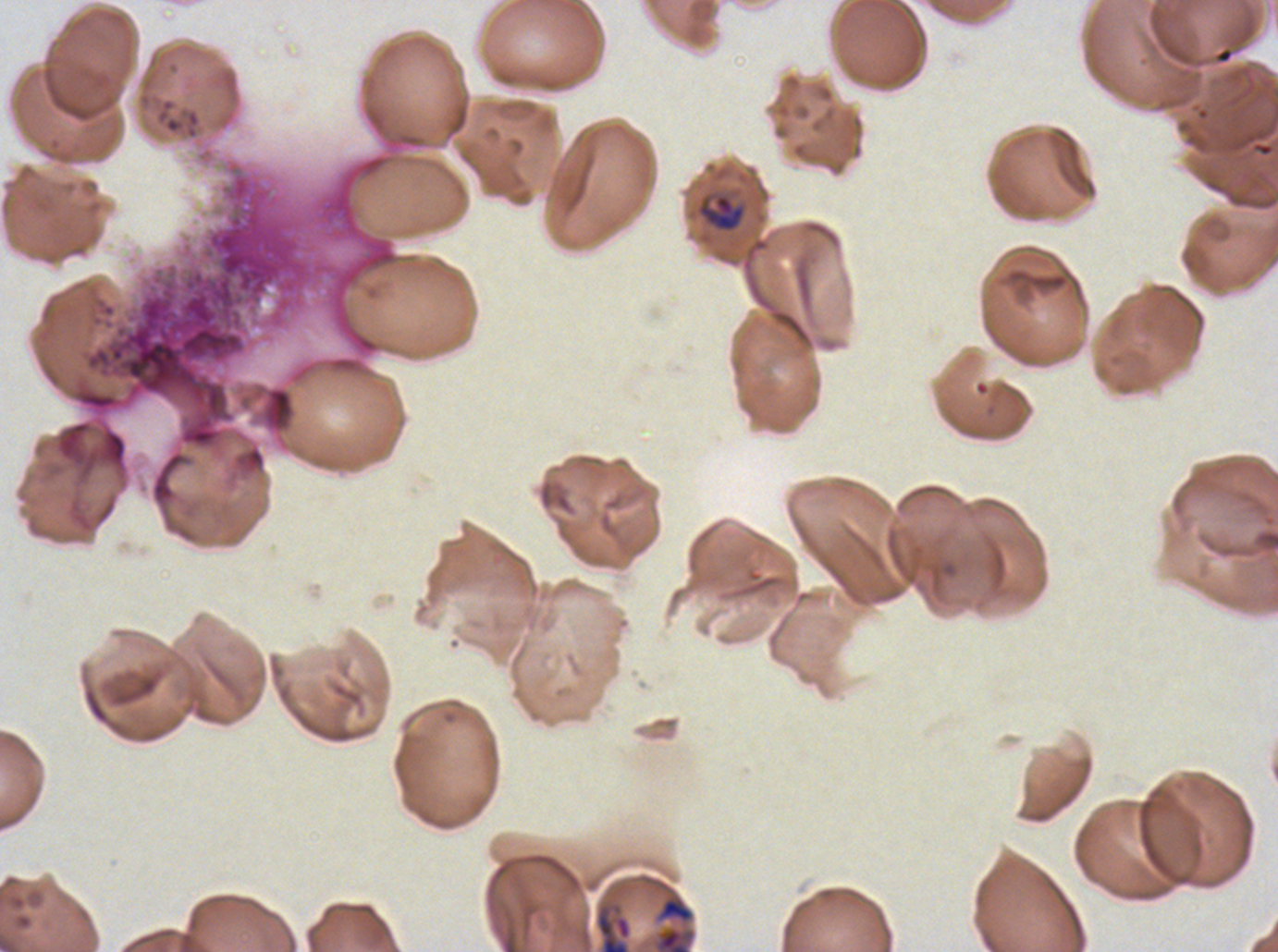

Approximate bounding boxes as (x1, y1, x2, y2) in pixels.
Summary:
  - Late-ring/early-trophozoite locations: (695, 192, 747, 233), (652, 924, 697, 951)
  - Stain: Giemsa
  - Specimen: P. falciparum cultured ex vivo for 24 to 48 hours, from a patient in The Gambia
  - Preparation: thin blood smear
  - Image size: 1278×952 pixels
  - Field of view: sub-image separated from a larger composite